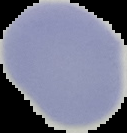
Summary:
  - Image size: 127×133 pixels
  - Image type: segmented cell region on a black background
  - Malaria status: uninfected
  - Preparation: thin blood film